Outline each Plasmodium vivax-infected red blood cell.
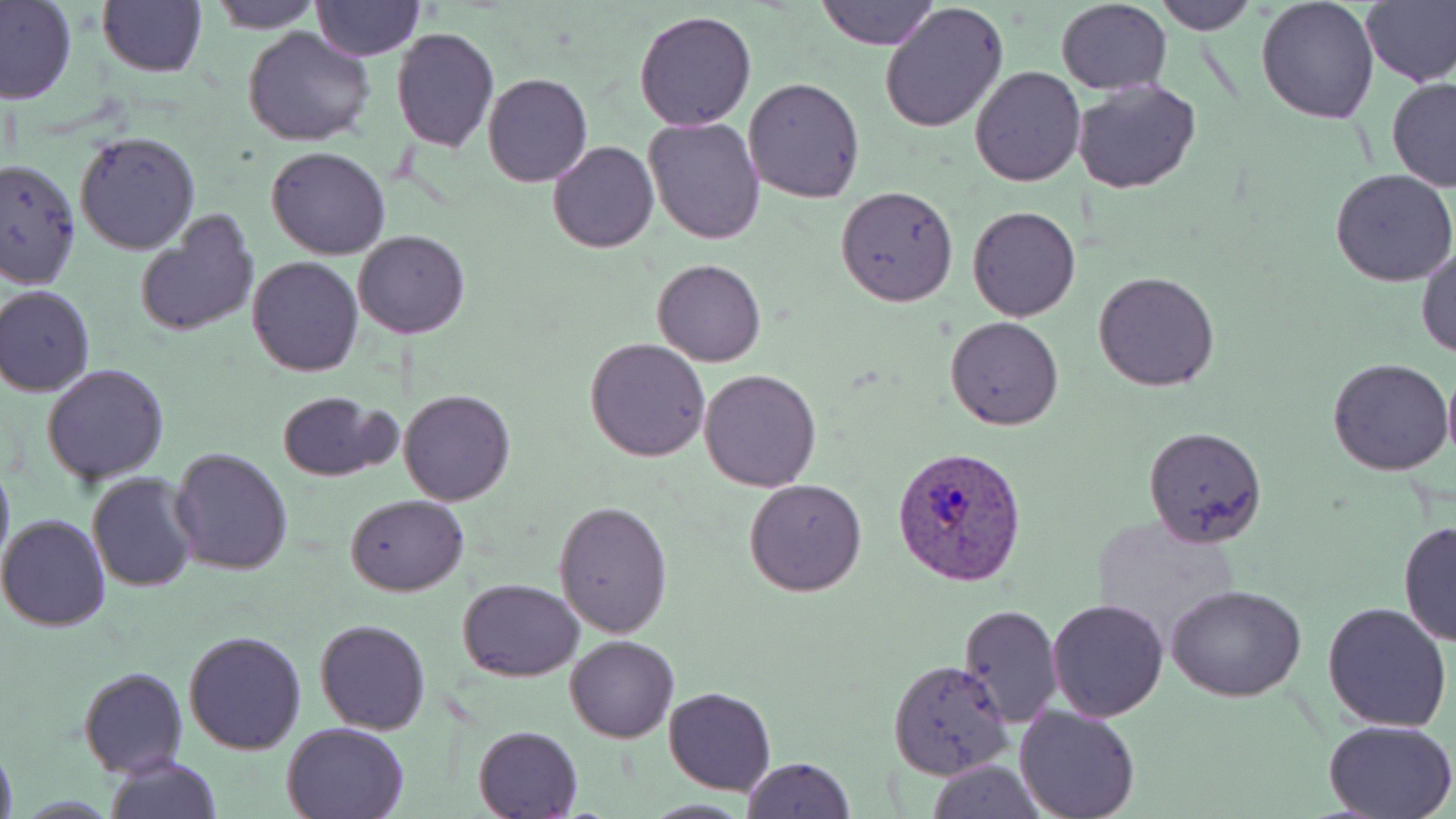
Approximate bounding boxes as named x1/y1/x2/y2 corners in pixels.
Plasmodium vivax-infected red blood cells: (x1=892, y1=446, x2=1028, y2=586).

{
  "slide_level_diagnosis": "Plasmodium vivax",
  "preparation": "thin blood film",
  "modality": "optical microscopy",
  "image_size": "1456×819 pixels",
  "stain": "May-Grünwald-Giemsa",
  "uninfected_red_blood_cell_locations": "approximate bounding boxes as named x1/y1/x2/y2 corners in pixels: (x1=0, y1=0, x2=77, y2=105), (x1=206, y1=0, x2=322, y2=33), (x1=817, y1=0, x2=936, y2=50), (x1=1257, y1=0, x2=1380, y2=123), (x1=1359, y1=0, x2=1456, y2=87), (x1=97, y1=1, x2=206, y2=78), (x1=311, y1=1, x2=423, y2=61), (x1=1151, y1=1, x2=1257, y2=35), (x1=878, y1=2, x2=1008, y2=135), (x1=1055, y1=2, x2=1171, y2=93), (x1=634, y1=9, x2=758, y2=131), (x1=243, y1=26, x2=376, y2=147), (x1=391, y1=27, x2=498, y2=153), (x1=969, y1=66, x2=1086, y2=186), (x1=483, y1=72, x2=592, y2=187), (x1=744, y1=77, x2=865, y2=205), (x1=1386, y1=77, x2=1456, y2=192), (x1=1072, y1=78, x2=1203, y2=194), (x1=644, y1=116, x2=765, y2=246), (x1=74, y1=131, x2=201, y2=254), (x1=548, y1=140, x2=659, y2=253), (x1=266, y1=147, x2=392, y2=260), (x1=0, y1=157, x2=79, y2=288), (x1=1330, y1=170, x2=1456, y2=288), (x1=835, y1=186, x2=958, y2=307), (x1=967, y1=206, x2=1081, y2=323), (x1=134, y1=212, x2=260, y2=340), (x1=353, y1=231, x2=469, y2=338), (x1=1416, y1=246, x2=1456, y2=361), (x1=246, y1=255, x2=363, y2=376), (x1=652, y1=258, x2=766, y2=367), (x1=1094, y1=271, x2=1219, y2=392), (x1=1, y1=286, x2=94, y2=397), (x1=944, y1=316, x2=1064, y2=430), (x1=585, y1=337, x2=710, y2=461), (x1=1328, y1=357, x2=1454, y2=475), (x1=42, y1=363, x2=169, y2=485), (x1=698, y1=369, x2=823, y2=492), (x1=1442, y1=370, x2=1456, y2=463), (x1=399, y1=389, x2=515, y2=506), (x1=276, y1=391, x2=397, y2=482), (x1=1142, y1=426, x2=1267, y2=549), (x1=170, y1=447, x2=292, y2=576), (x1=0, y1=455, x2=14, y2=579), (x1=87, y1=471, x2=199, y2=593), (x1=745, y1=478, x2=867, y2=597), (x1=345, y1=495, x2=469, y2=596), (x1=554, y1=499, x2=673, y2=637), (x1=0, y1=513, x2=111, y2=633), (x1=1087, y1=514, x2=1243, y2=644), (x1=1398, y1=520, x2=1455, y2=647), (x1=459, y1=579, x2=584, y2=681), (x1=1166, y1=585, x2=1308, y2=702), (x1=1046, y1=598, x2=1170, y2=721), (x1=1321, y1=603, x2=1452, y2=734), (x1=958, y1=605, x2=1062, y2=725), (x1=315, y1=619, x2=431, y2=735), (x1=183, y1=629, x2=307, y2=754), (x1=566, y1=635, x2=678, y2=742), (x1=887, y1=659, x2=1013, y2=781), (x1=77, y1=666, x2=187, y2=777), (x1=664, y1=687, x2=776, y2=795), (x1=1015, y1=705, x2=1142, y2=819), (x1=1324, y1=718, x2=1456, y2=818), (x1=282, y1=721, x2=409, y2=819), (x1=473, y1=725, x2=582, y2=819), (x1=0, y1=739, x2=17, y2=819), (x1=104, y1=756, x2=221, y2=819), (x1=740, y1=757, x2=854, y2=819), (x1=926, y1=760, x2=1046, y2=818)",
  "field_of_view": "single",
  "magnification": "1000x"
}